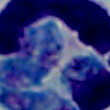
magnification = 1000x
modality = micrograph
identification = leukocyte